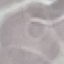

result: no malaria parasites detected
stain: Giemsa
preparation: thin blood film
image_type: automatically extracted cell patch, resized to 64 × 64 pixels
capture: smartphone camera at the microscope eyepiece